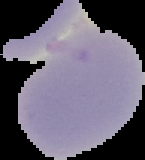

preparation = thin blood smear
result = no Plasmodium parasites seen
image type = segmented cell region on a black background
image size = 145×160 pixels